Assess the morphology of the red blood cells.
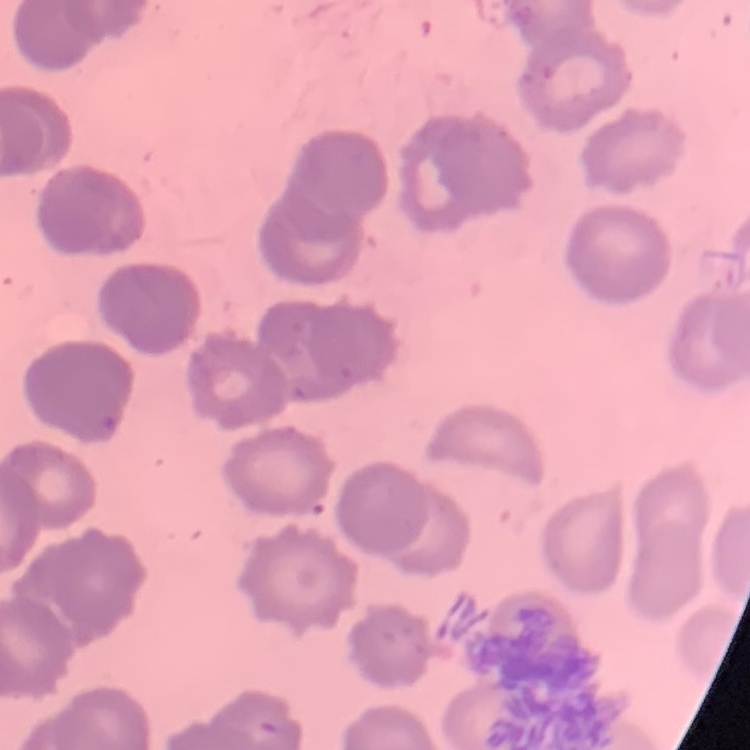

They show rouleaux formation.

Thin blood film. Stained with either Field's or Giemsa. Square crop of a larger photomicrograph.